State which parasite is depicted.
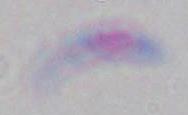
Toxoplasma gondii.

modality: micrograph
magnification: 1000x